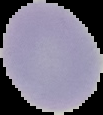

Summary:
  - Preparation: thin blood film
  - Image size: 103×115 pixels
  - Image type: cell region segmented out of the field of view; surrounding area masked to black
  - Malaria status: uninfected